State which parasite is depicted.
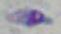

This is Toxoplasma gondii.

magnification = 1000x
modality = micrograph